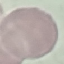

Summary:
  - Result: no malaria parasites seen
  - Image type: automatically extracted cell patch, resized to 64 × 64 pixels
  - Capture: smartphone camera at the microscope eyepiece
  - Preparation: thin blood smear
  - Stain: Giemsa